Identify the blood parasite species.
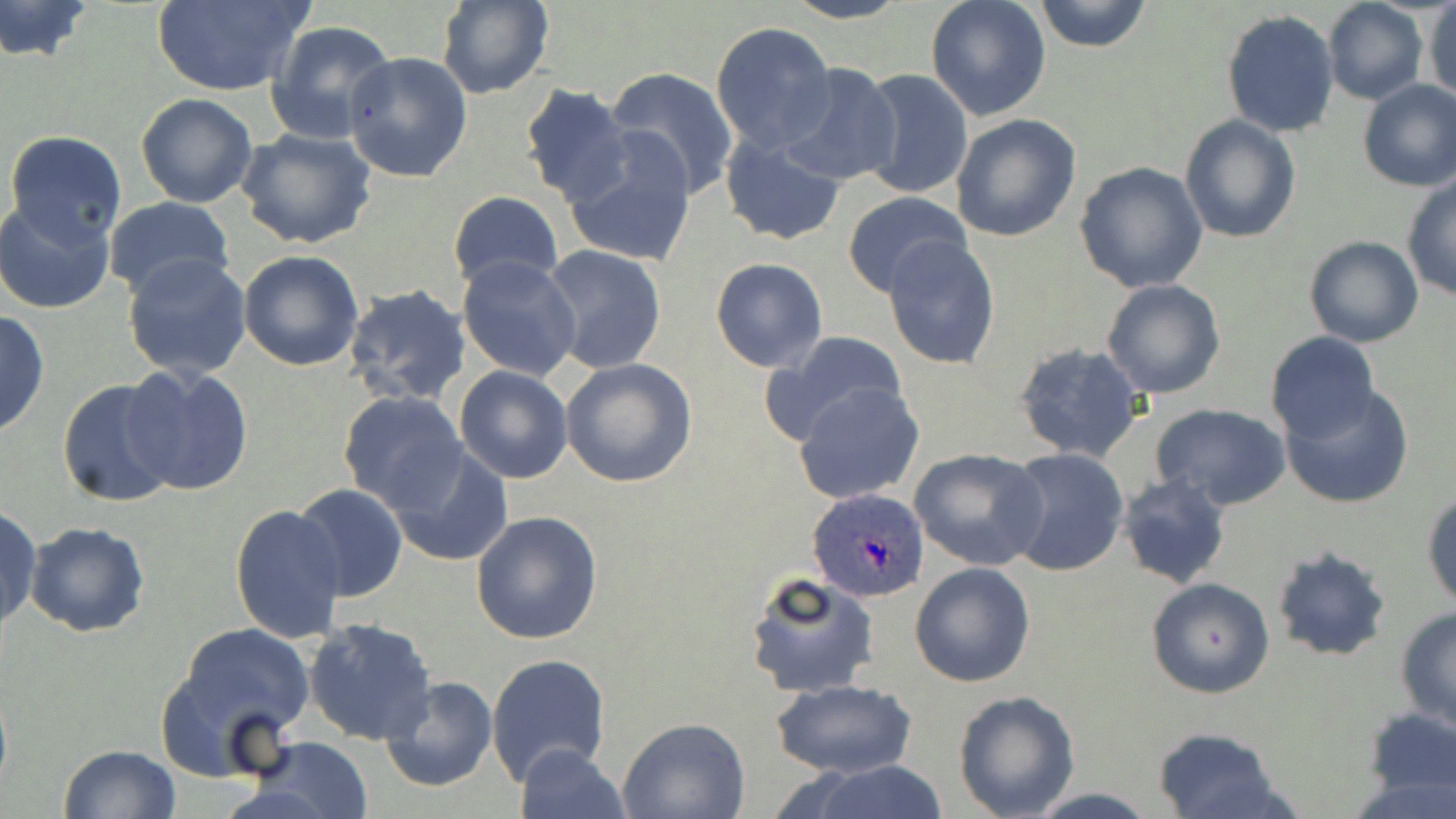

Plasmodium ovale.

Summary:
  - Coordinate format: approximate bounding boxes as [x1, y1, x2, y2] in pixels
  - Uninfected red blood cell locations: [0, 0, 94, 63], [777, 0, 917, 25], [925, 0, 1053, 121], [1034, 0, 1151, 52], [150, 1, 313, 95], [435, 1, 554, 99], [1322, 1, 1429, 105], [1423, 2, 1456, 103], [1222, 9, 1340, 137], [264, 19, 395, 143], [710, 20, 836, 153], [343, 50, 473, 181], [778, 64, 904, 186], [602, 67, 736, 197], [856, 68, 974, 200], [1356, 78, 1456, 192], [518, 85, 636, 208], [135, 93, 257, 208], [949, 113, 1082, 242], [1180, 114, 1301, 244], [235, 127, 377, 249], [4, 129, 128, 246], [560, 132, 700, 268], [719, 134, 846, 245], [1074, 162, 1208, 292], [1402, 177, 1456, 301], [447, 190, 563, 290], [842, 190, 972, 297], [0, 197, 117, 315], [103, 197, 235, 302], [882, 233, 1002, 370], [1303, 237, 1424, 349], [542, 245, 667, 373], [238, 250, 364, 371], [122, 252, 253, 379], [457, 255, 582, 380], [710, 257, 828, 373], [1102, 278, 1226, 399], [344, 283, 472, 406], [0, 308, 50, 440], [759, 329, 912, 448], [1264, 332, 1381, 445], [1011, 340, 1149, 463], [560, 358, 697, 487], [124, 364, 255, 500], [454, 365, 574, 484], [56, 376, 185, 508], [353, 379, 571, 507], [1278, 380, 1415, 510], [794, 382, 924, 505], [337, 392, 470, 514], [1150, 405, 1291, 511], [388, 444, 515, 567], [909, 447, 1047, 571], [1002, 448, 1129, 578], [1126, 470, 1243, 698], [1116, 473, 1233, 590], [292, 485, 407, 601], [1423, 489, 1455, 610], [230, 503, 346, 644], [0, 504, 41, 633], [471, 511, 603, 645], [24, 522, 149, 638], [1270, 544, 1392, 662], [910, 561, 1036, 687], [743, 569, 879, 699], [1145, 576, 1275, 699], [1394, 610, 1456, 735], [304, 617, 437, 744], [166, 622, 316, 766], [486, 652, 610, 785], [379, 675, 498, 793], [770, 678, 919, 779], [951, 690, 1080, 819], [1361, 703, 1456, 805], [617, 717, 749, 819], [1150, 726, 1289, 819], [245, 735, 374, 819], [58, 744, 181, 819], [514, 744, 628, 819], [794, 762, 953, 819]
  - Plasmodium ovale-infected red blood cell locations: [806, 486, 930, 602]
  - Preparation: thin blood film
  - Stain: May-Grünwald-Giemsa
  - Magnification: 1000x
  - Modality: light microscopy
  - Field of view: single
  - Image size: 1456×819 pixels